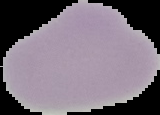 From a thin blood film. Malaria status: uninfected. Image is 160×115 pixels. Segmented cell region on a black background.